Give the extent of all Babesia divergens-infected red blood cells.
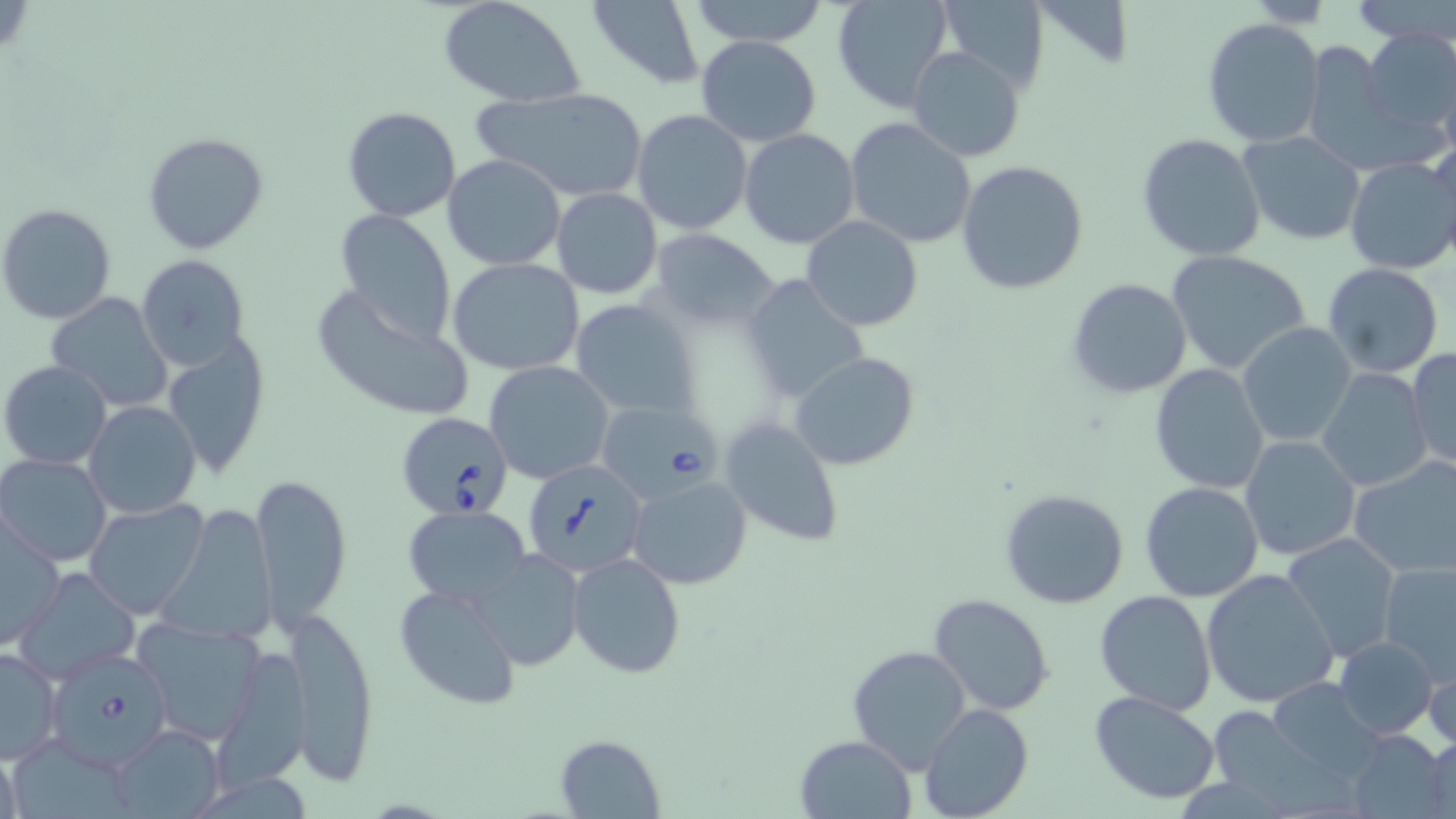
Approximate bounding boxes as (x1, y1, x2, y2) in pixels.
Babesia divergens-infected red blood cells: (597, 395, 733, 506), (395, 413, 516, 517), (525, 458, 648, 578), (46, 653, 171, 772).

slide-level diagnosis = Babesia divergens
magnification = 1000x
preparation = thin blood smear
field of view = one of a larger specimen
uninfected red blood cell locations = approximate bounding boxes as (x1, y1, x2, y2) in pixels: (438, 0, 587, 108), (587, 0, 706, 88), (682, 0, 832, 48), (832, 0, 957, 113), (934, 0, 1050, 95), (1345, 0, 1456, 45), (1202, 17, 1327, 149), (1360, 26, 1456, 143), (695, 35, 822, 147), (1300, 40, 1411, 172), (906, 46, 1025, 162), (477, 88, 649, 202), (341, 106, 461, 223), (631, 109, 753, 235), (846, 118, 978, 249), (738, 128, 860, 249), (142, 131, 268, 254), (1237, 131, 1367, 244), (1137, 134, 1267, 262), (1429, 138, 1456, 268), (442, 154, 568, 272), (1343, 156, 1456, 275), (956, 160, 1089, 295), (550, 188, 663, 299), (1, 203, 116, 324), (333, 210, 458, 343), (801, 216, 923, 332), (648, 230, 779, 330), (1166, 249, 1311, 375), (136, 254, 249, 369), (448, 258, 586, 374), (1322, 263, 1444, 378), (740, 275, 873, 405), (1066, 277, 1192, 400), (310, 290, 477, 423), (46, 293, 173, 412), (568, 299, 700, 419), (1237, 322, 1357, 448), (163, 336, 269, 478), (1407, 346, 1456, 473), (789, 351, 919, 470), (1, 360, 113, 471), (484, 361, 616, 484), (1150, 363, 1270, 493), (1317, 368, 1430, 492), (83, 400, 201, 518), (718, 415, 844, 546), (1240, 435, 1362, 560), (0, 454, 115, 567), (1349, 454, 1456, 581), (251, 472, 352, 628), (627, 475, 751, 590), (1139, 482, 1265, 602), (999, 488, 1129, 609), (85, 500, 208, 620), (160, 505, 279, 641), (401, 506, 531, 606), (1, 516, 64, 649), (1283, 534, 1402, 662), (473, 547, 585, 669), (566, 552, 685, 678), (1377, 561, 1456, 686), (15, 566, 141, 683), (1201, 569, 1339, 708), (395, 583, 524, 711), (1095, 589, 1217, 716), (928, 592, 1056, 716), (283, 604, 380, 784), (133, 616, 267, 746), (1335, 636, 1439, 739), (0, 645, 63, 764), (216, 646, 312, 787), (846, 646, 972, 773), (1423, 650, 1456, 752), (1271, 678, 1383, 778), (1089, 691, 1220, 805), (920, 703, 1034, 819), (1211, 709, 1317, 800), (106, 725, 226, 818), (1353, 730, 1449, 816), (1417, 732, 1456, 817), (553, 734, 665, 817), (796, 734, 915, 817), (13, 743, 127, 819)
stain = May-Grünwald-Giemsa
modality = light microscopy
image size = 1456×819 pixels